State which cell type is depicted.
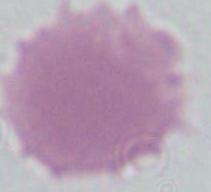
This is an erythrocyte.

Micrograph. Captured at 1000x magnification.